Report the malaria status of this cell.
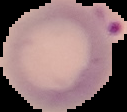
It is parasitized.

From a thin blood film. Image is 127×112 pixels. Cell region segmented out of the field of view; the surrounding area is masked to black.